Name the parasite shown.
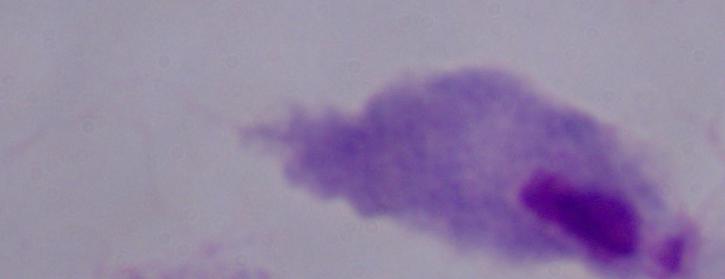

This is a trichomonad.

Micrograph. 1000x magnification.